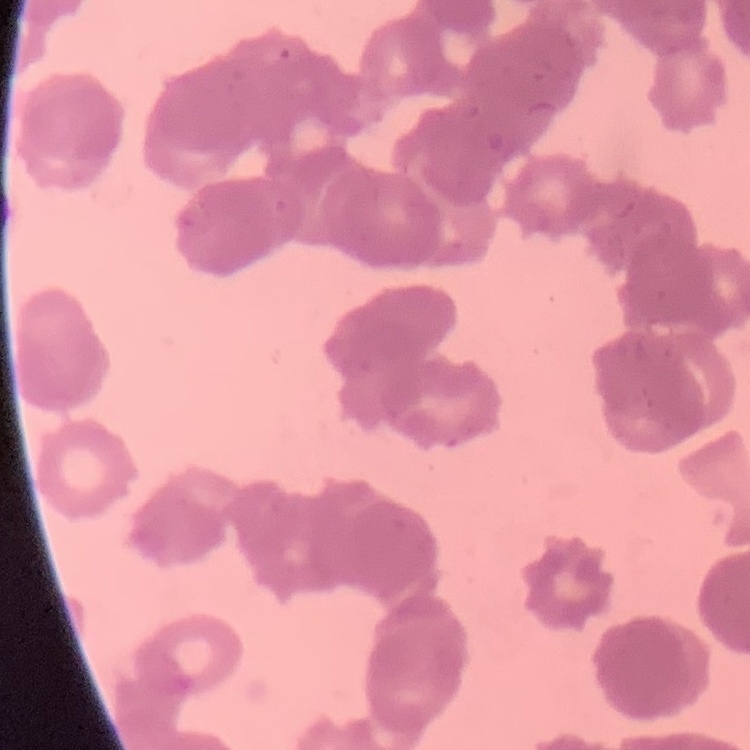

Summary:
  - Erythrocyte morphology: rouleaux formation
  - Image type: square crop of a larger photomicrograph
  - Preparation: thin blood film
  - Stain: Field's or Giemsa